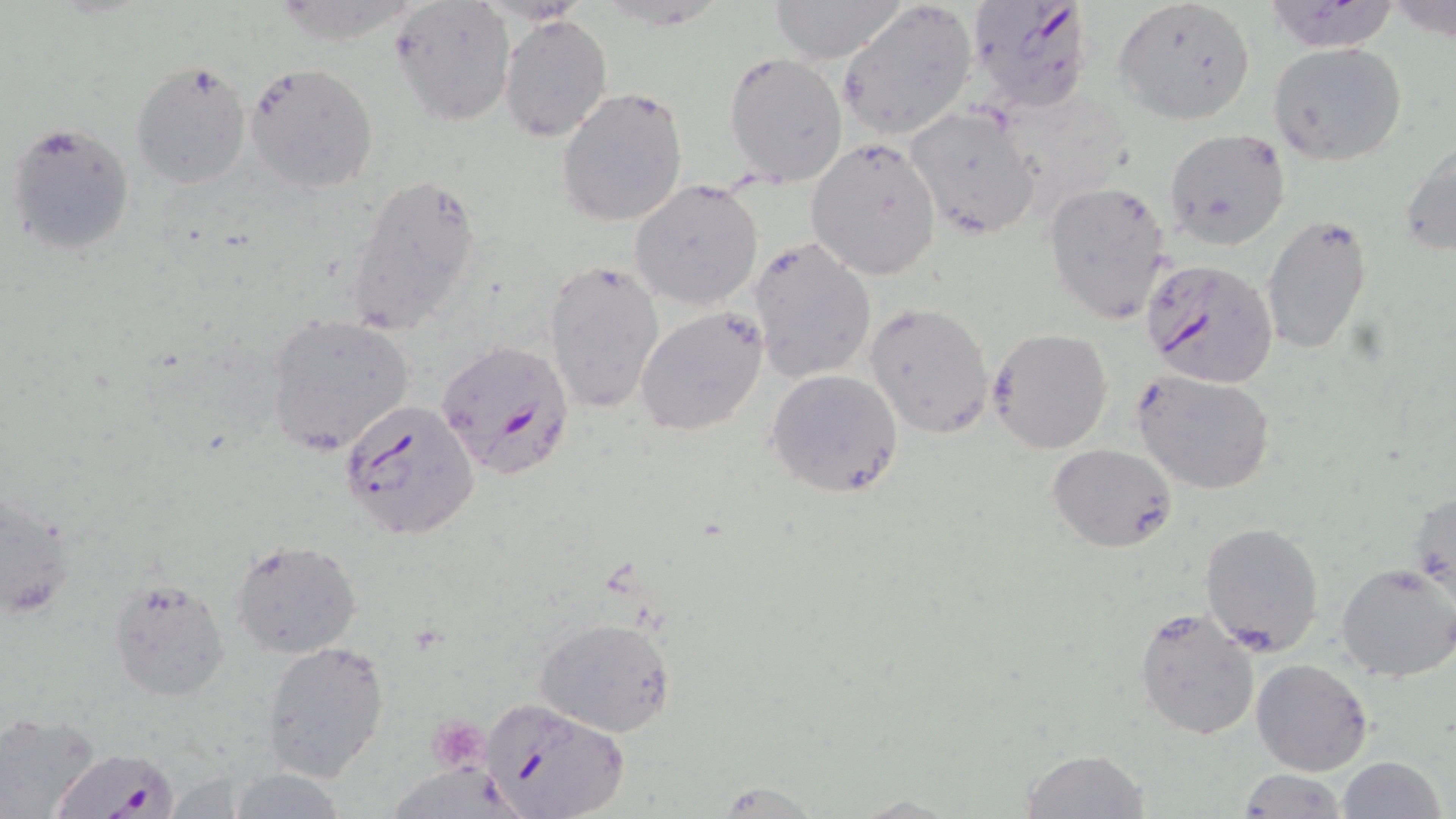
Summary:
  - Coordinate format: approximate bounding boxes as named x1/y1/x2/y2 corners in pixels
  - Plasmodium falciparum-infected red blood cell locations: (x1=966, y1=0, x2=1095, y2=117), (x1=1141, y1=258, x2=1279, y2=388), (x1=434, y1=340, x2=575, y2=479), (x1=341, y1=400, x2=480, y2=541), (x1=479, y1=698, x2=630, y2=819), (x1=57, y1=747, x2=175, y2=819)
  - Uninfected red blood cell locations: (x1=764, y1=0, x2=908, y2=63), (x1=1113, y1=0, x2=1255, y2=126), (x1=835, y1=1, x2=978, y2=141), (x1=1261, y1=1, x2=1406, y2=52), (x1=392, y1=2, x2=517, y2=125), (x1=501, y1=16, x2=612, y2=141), (x1=1266, y1=41, x2=1408, y2=166), (x1=724, y1=53, x2=848, y2=186), (x1=129, y1=58, x2=252, y2=188), (x1=245, y1=63, x2=378, y2=196), (x1=557, y1=88, x2=689, y2=227), (x1=904, y1=107, x2=1041, y2=239), (x1=6, y1=122, x2=136, y2=257), (x1=1162, y1=128, x2=1292, y2=250), (x1=1400, y1=137, x2=1456, y2=258), (x1=805, y1=138, x2=942, y2=280), (x1=344, y1=169, x2=483, y2=336), (x1=631, y1=180, x2=764, y2=309), (x1=1044, y1=180, x2=1174, y2=327), (x1=1260, y1=213, x2=1373, y2=359), (x1=749, y1=238, x2=876, y2=384), (x1=544, y1=259, x2=665, y2=414), (x1=865, y1=302, x2=995, y2=437), (x1=634, y1=306, x2=769, y2=435), (x1=266, y1=316, x2=414, y2=457), (x1=988, y1=328, x2=1113, y2=454), (x1=767, y1=368, x2=905, y2=498), (x1=1133, y1=370, x2=1278, y2=495), (x1=1048, y1=443, x2=1177, y2=553), (x1=1410, y1=484, x2=1455, y2=605), (x1=1198, y1=522, x2=1325, y2=657), (x1=228, y1=538, x2=365, y2=660), (x1=1335, y1=563, x2=1456, y2=682), (x1=108, y1=579, x2=230, y2=701), (x1=1133, y1=607, x2=1260, y2=740), (x1=534, y1=616, x2=677, y2=738), (x1=260, y1=638, x2=391, y2=782), (x1=1250, y1=658, x2=1373, y2=776), (x1=0, y1=710, x2=101, y2=818), (x1=1020, y1=748, x2=1152, y2=818), (x1=1337, y1=756, x2=1446, y2=819), (x1=224, y1=767, x2=348, y2=819), (x1=1237, y1=769, x2=1348, y2=818)
  - Platelet locations: (x1=429, y1=717, x2=490, y2=773)
  - Slide-level diagnosis: Plasmodium falciparum
  - Image size: 1456×819 pixels
  - Preparation: thin blood film
  - Magnification: 1000x
  - Modality: optical microscopy
  - Stain: May-Grünwald-Giemsa
  - Field of view: one of a larger specimen